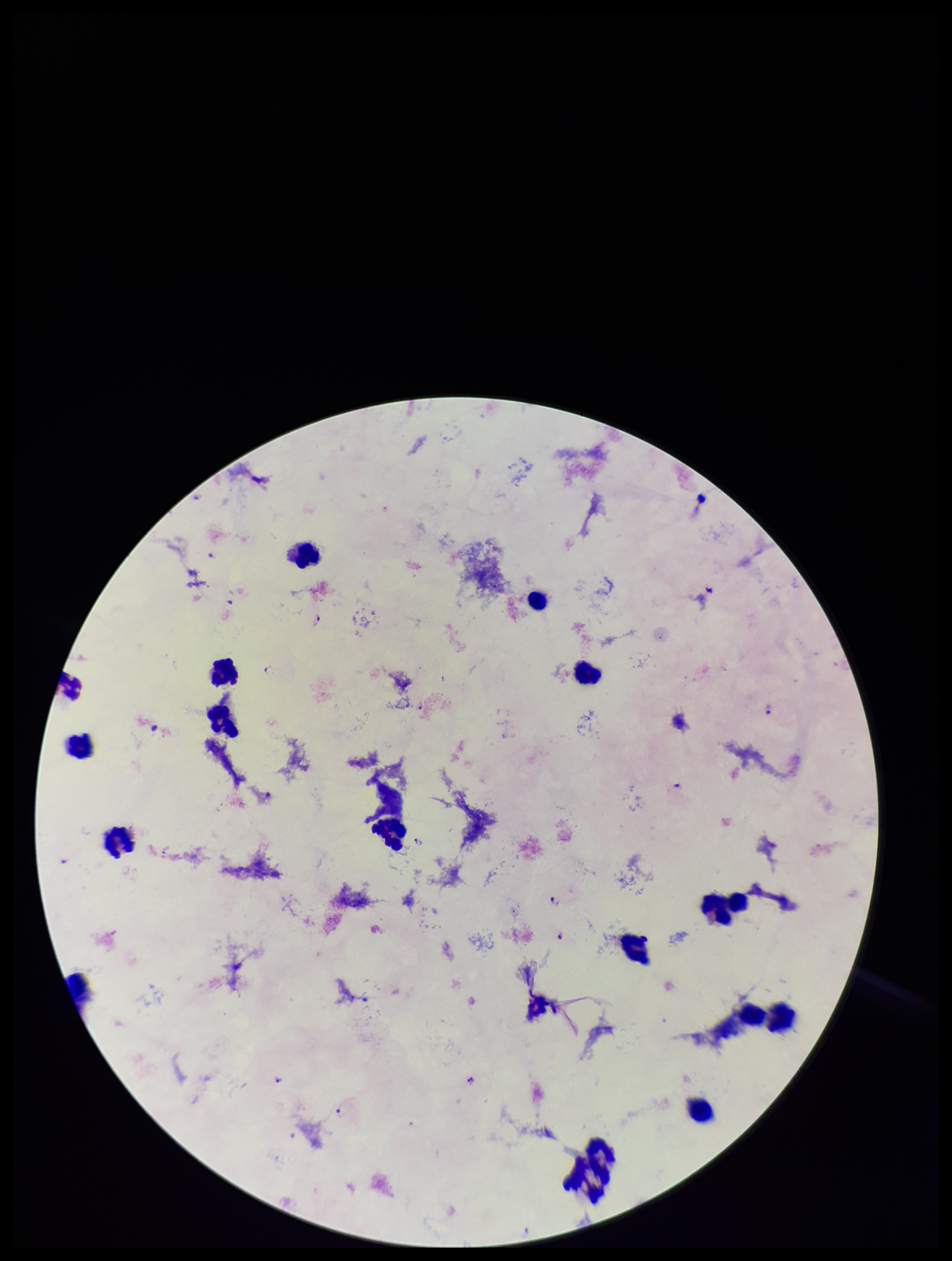

image_size: 952×1261 pixels
parasite_count: 13
capture: smartphone photograph through the microscope eyepiece
species_reported_for_this_patient: Plasmodium falciparum
preparation: thick smear
stain: Giemsa
leukocyte_count: 16
field_of_view: one from this slide
plasmodium_parasites: seen
patient_malaria_status: positive